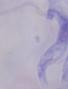

1000x magnification. A trypanosome is seen. Photomicrograph.